Report the malaria status of this cell.
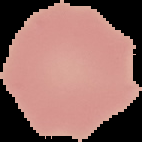
It is uninfected.

Summary:
  - Preparation: thin blood smear
  - Image size: 142×142 pixels
  - Image type: cell region segmented out of the field of view; surrounding area masked to black